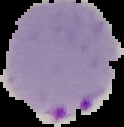

Summary:
  - Preparation: thin blood smear
  - Image size: 124×127 pixels
  - Malaria status: parasitized
  - Image type: segmented cell region with the area outside set to black